Assess the morphology of the erythrocytes.
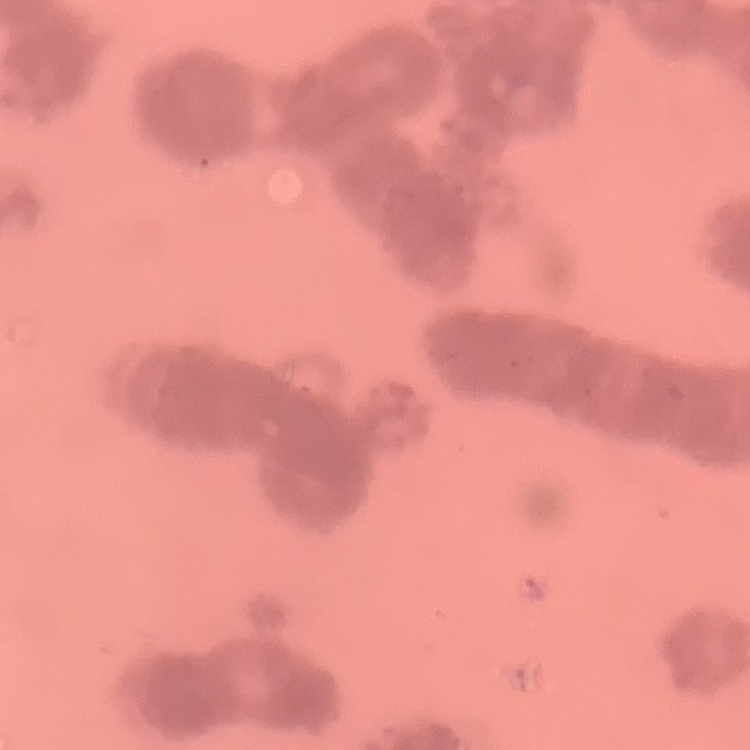
Rouleaux formation.

Thin blood film. Square crop of a larger photomicrograph. Field's or Giemsa stain.